Assess the morphology of the red blood cells.
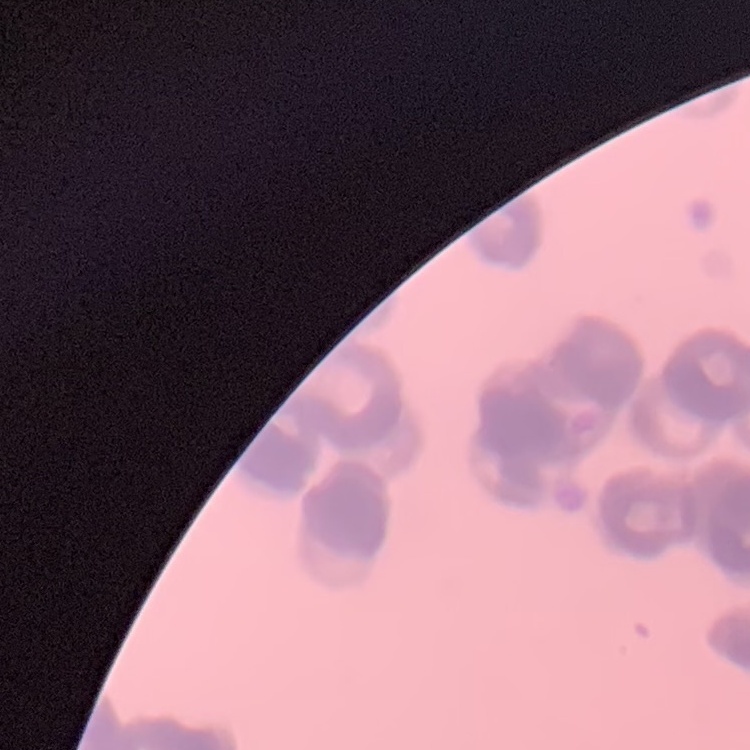

Rouleaux formation.

Stained with either Field's or Giemsa. One tile cut from a larger photomicrograph. Thin peripheral smear.